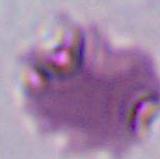

magnification = 400x or 1000x
identification = Plasmodium
modality = photomicrograph